Classify this cell by malaria status.
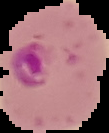

It is parasitized.

Summary:
  - Preparation: thin blood smear
  - Image type: cell region segmented out of the field of view; surrounding area masked to black
  - Image size: 109×133 pixels